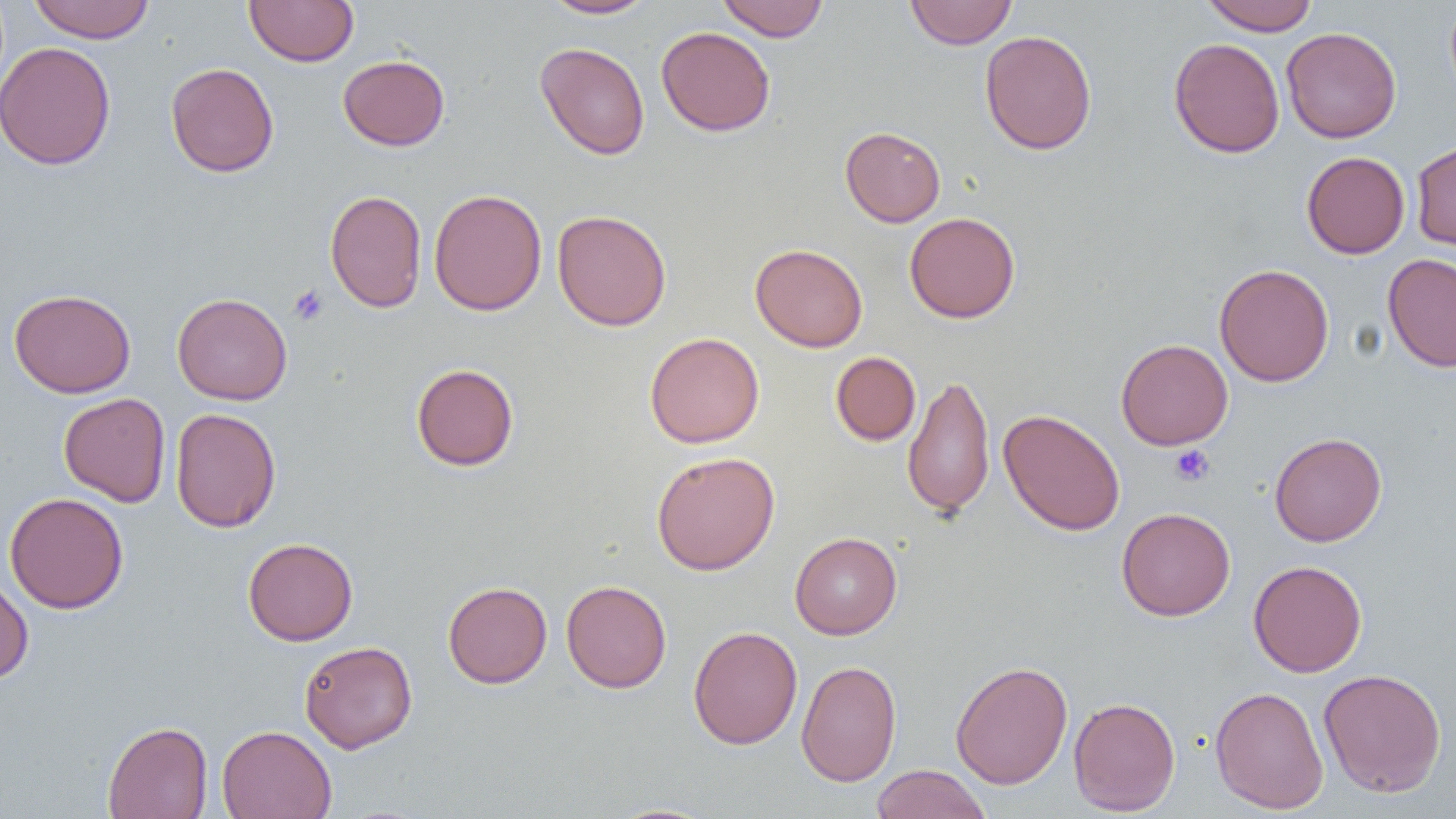
Approximate bounding boxes as (x1,y1)-(x2,y2) corner pairs in pixels. Uninfected red blood cell locations: (244,0)-(359,67), (541,0)-(656,19), (716,0)-(829,41), (905,0)-(1017,49), (1200,0)-(1319,35), (28,1)-(155,43), (656,27)-(775,136), (1281,27)-(1401,143), (980,29)-(1097,155), (1169,38)-(1285,158), (0,41)-(117,170), (535,42)-(650,160), (337,54)-(450,151), (165,62)-(279,177), (840,126)-(945,227), (1411,140)-(1456,255), (1301,151)-(1410,258), (429,188)-(547,316), (325,189)-(427,313), (552,209)-(671,331), (904,212)-(1020,323), (750,243)-(868,352), (1383,253)-(1456,373), (1213,263)-(1334,387), (9,288)-(136,398), (172,292)-(292,405), (645,332)-(765,448), (1116,338)-(1233,450), (830,351)-(921,445), (411,363)-(519,471), (903,374)-(995,518), (58,393)-(171,507), (170,408)-(282,533), (998,409)-(1126,536), (1269,431)-(1387,546), (651,451)-(780,575), (4,492)-(129,614), (1116,506)-(1236,621), (790,532)-(902,639), (243,537)-(358,645), (1248,559)-(1367,677), (0,577)-(34,682), (561,579)-(672,693), (442,581)-(552,688), (687,625)-(803,749), (300,640)-(418,753), (796,660)-(901,787), (950,660)-(1073,789), (1318,668)-(1447,798), (1210,685)-(1328,815), (1068,696)-(1181,816), (102,720)-(213,819), (217,725)-(336,818), (870,764)-(992,819), (602,803)-(724,819). Platelet locations: (288,284)-(328,326), (1170,444)-(1215,486). Slide-level diagnosis: negative for blood parasites. 1000x magnification. Thin blood film. Single field of view. Image is 1456×819 pixels. Light microscopy.